Classify this cell by malaria status.
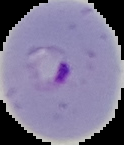
Parasitized.

{
  "image_type": "segmented cell region on a black background",
  "image_size": "124×145 pixels",
  "preparation": "thin blood smear"
}